Locate every white blood cell.
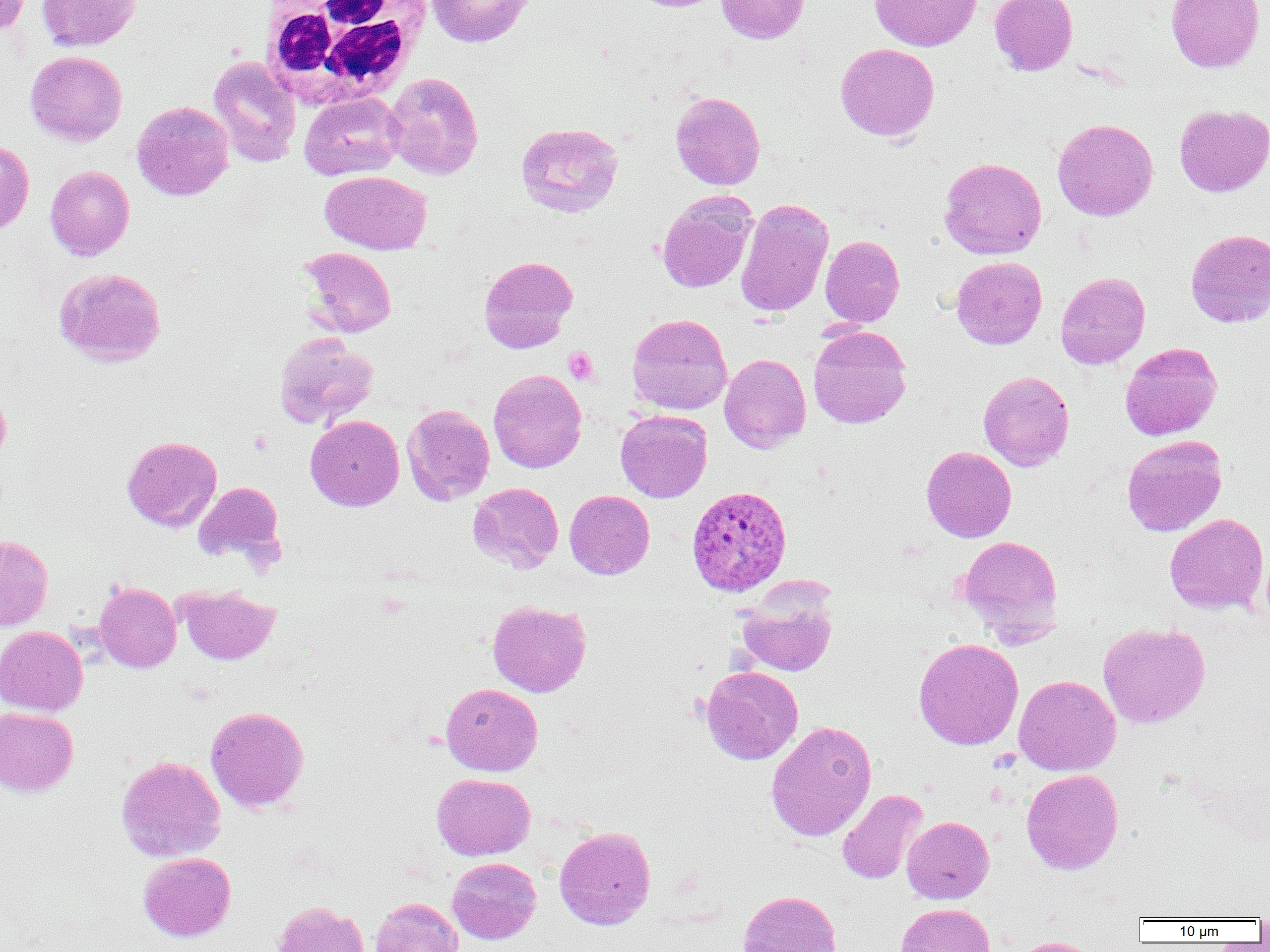

Approximate bounding boxes as named x1/y1/x2/y2 corners in pixels.
White blood cells: (x1=257, y1=0, x2=433, y2=106).

Summary:
  - Uninfected red blood cell locations: (x1=0, y1=0, x2=31, y2=34), (x1=37, y1=0, x2=141, y2=52), (x1=426, y1=0, x2=535, y2=48), (x1=628, y1=0, x2=726, y2=13), (x1=716, y1=0, x2=810, y2=44), (x1=869, y1=0, x2=982, y2=52), (x1=989, y1=0, x2=1078, y2=75), (x1=1165, y1=0, x2=1265, y2=73), (x1=835, y1=43, x2=939, y2=142), (x1=25, y1=51, x2=127, y2=145), (x1=208, y1=55, x2=301, y2=168), (x1=383, y1=72, x2=484, y2=180), (x1=670, y1=91, x2=766, y2=190), (x1=298, y1=92, x2=404, y2=181), (x1=132, y1=101, x2=234, y2=201), (x1=1173, y1=104, x2=1270, y2=197), (x1=1052, y1=118, x2=1158, y2=221), (x1=516, y1=122, x2=623, y2=218), (x1=0, y1=140, x2=34, y2=236), (x1=939, y1=158, x2=1047, y2=259), (x1=45, y1=165, x2=134, y2=261), (x1=320, y1=171, x2=432, y2=254), (x1=656, y1=191, x2=756, y2=294), (x1=735, y1=199, x2=834, y2=317), (x1=1185, y1=228, x2=1270, y2=328), (x1=820, y1=235, x2=905, y2=327), (x1=298, y1=246, x2=397, y2=338), (x1=478, y1=255, x2=578, y2=353), (x1=951, y1=256, x2=1047, y2=349), (x1=53, y1=267, x2=166, y2=367), (x1=1055, y1=272, x2=1150, y2=369), (x1=626, y1=313, x2=733, y2=415), (x1=808, y1=325, x2=912, y2=428), (x1=274, y1=333, x2=378, y2=429), (x1=1119, y1=342, x2=1222, y2=441), (x1=719, y1=353, x2=811, y2=452), (x1=488, y1=369, x2=587, y2=473), (x1=978, y1=371, x2=1075, y2=471), (x1=0, y1=389, x2=11, y2=467), (x1=401, y1=404, x2=495, y2=505), (x1=615, y1=410, x2=712, y2=502), (x1=305, y1=415, x2=404, y2=511), (x1=1121, y1=435, x2=1227, y2=536), (x1=121, y1=436, x2=222, y2=532), (x1=921, y1=446, x2=1016, y2=542), (x1=193, y1=482, x2=284, y2=563), (x1=467, y1=482, x2=563, y2=573), (x1=564, y1=490, x2=655, y2=580), (x1=1164, y1=513, x2=1269, y2=615), (x1=0, y1=535, x2=53, y2=631), (x1=958, y1=535, x2=1064, y2=642), (x1=94, y1=582, x2=181, y2=672), (x1=177, y1=585, x2=280, y2=665), (x1=737, y1=591, x2=837, y2=676), (x1=487, y1=601, x2=591, y2=697), (x1=1097, y1=622, x2=1210, y2=728), (x1=0, y1=626, x2=88, y2=716), (x1=913, y1=638, x2=1024, y2=750), (x1=701, y1=666, x2=803, y2=764), (x1=1013, y1=674, x2=1121, y2=776), (x1=440, y1=683, x2=543, y2=776), (x1=205, y1=706, x2=309, y2=813), (x1=0, y1=707, x2=78, y2=797), (x1=766, y1=720, x2=877, y2=841), (x1=115, y1=756, x2=226, y2=862), (x1=1021, y1=769, x2=1123, y2=874), (x1=431, y1=773, x2=535, y2=861), (x1=837, y1=789, x2=929, y2=884), (x1=901, y1=816, x2=994, y2=904), (x1=554, y1=825, x2=656, y2=930), (x1=138, y1=852, x2=236, y2=942), (x1=447, y1=857, x2=541, y2=944), (x1=739, y1=890, x2=841, y2=952), (x1=370, y1=897, x2=464, y2=952), (x1=271, y1=900, x2=371, y2=952), (x1=895, y1=903, x2=995, y2=952), (x1=1007, y1=936, x2=1103, y2=952)
  - Plasmodium ovale-infected red blood cell locations: (x1=686, y1=485, x2=792, y2=596)
  - Platelet locations: (x1=563, y1=347, x2=599, y2=385), (x1=249, y1=430, x2=272, y2=455)
  - Slide-level diagnosis: Plasmodium ovale
  - Modality: light microscopy
  - Image size: 1270×952 pixels
  - Preparation: thin blood smear
  - Magnification: 1000x
  - Field of view: one of a larger specimen